Give the position of every Plasmodium parasite.
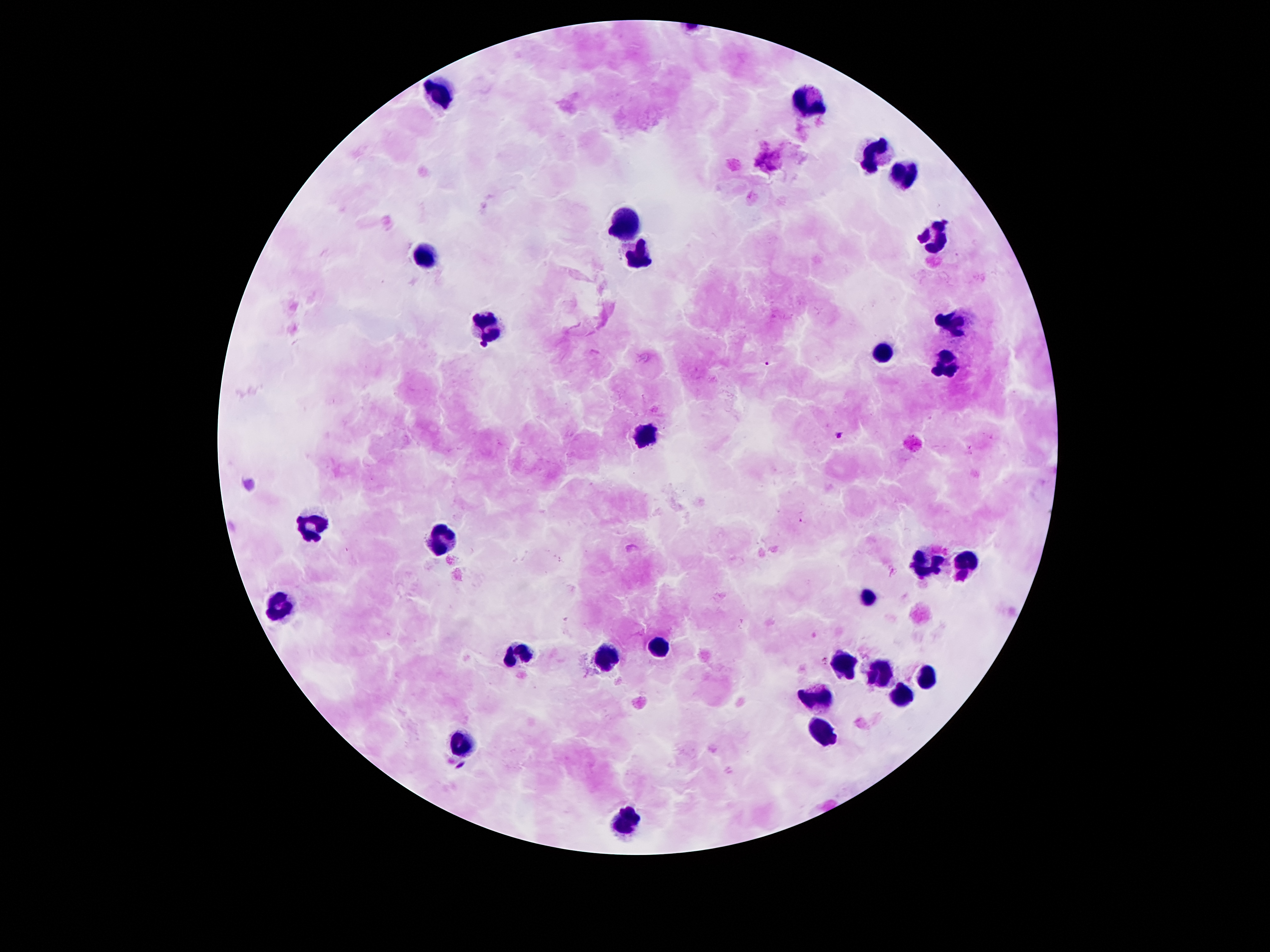
Approximate centers as (x, y) in pixels.
Plasmodium parasites: (766, 365), (838, 434), (460, 765).

Leukocyte locations: (433, 94), (804, 101), (872, 154), (903, 173), (623, 222), (932, 237), (421, 251), (638, 258), (948, 323), (488, 326), (881, 354), (941, 362), (643, 435), (309, 525), (441, 538), (963, 560), (925, 564), (868, 600), (278, 606), (660, 644), (514, 651), (605, 660), (842, 664), (877, 672), (928, 673), (813, 697), (899, 697), (824, 730), (459, 741), (625, 823). One field from this slide. Patient malaria status: positive for Plasmodium falciparum. Giemsa-stained preparation. Smartphone photograph taken through the microscope eyepiece. 100x magnification. Image is 1270×952 pixels. Thick peripheral-blood smear.